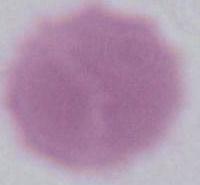 Captured at 1000x magnification. Micrograph. An erythrocyte is seen.